Assess this cell for malaria.
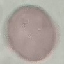

It is uninfected.

Summary:
  - Stain: Giemsa
  - Capture: smartphone through the microscope eyepiece
  - Preparation: thin smear
  - Image type: cell patch, automatically extracted from a larger field of view and resized to 64 × 64 pixels